Locate every malaria parasite and every leukocyte.
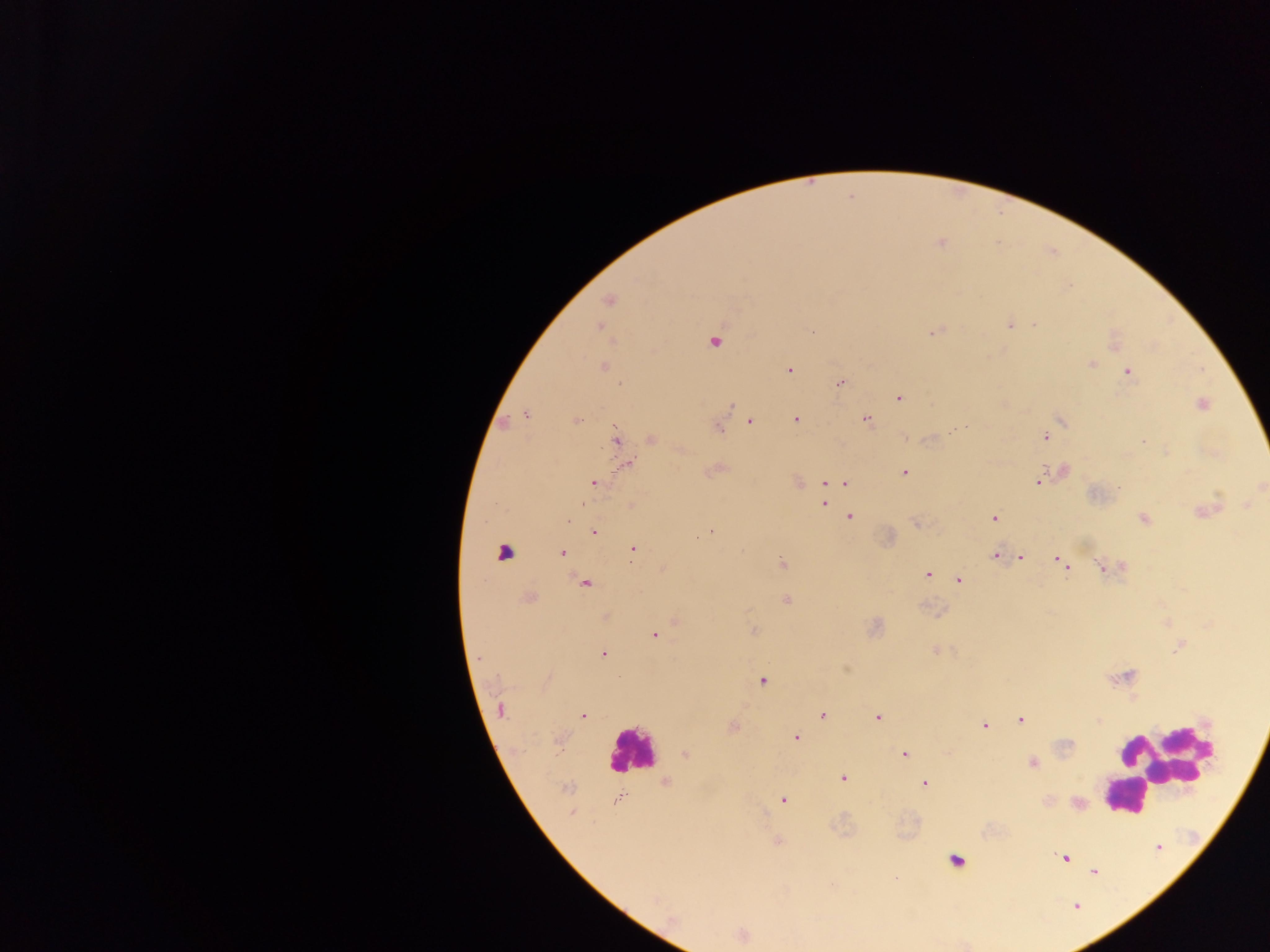
Approximate centers as x y in pixels.
Malaria parasites: 940 243; 609 301; 1009 325; 1035 325; 599 327; 932 332; 713 341; 1090 365; 604 367; 790 370; 1128 372; 841 383; 899 397; 1202 404; 731 405; 525 414; 796 419; 577 420; 866 420; 749 421; 1060 421; 717 428; 1046 437; 615 438; 652 439; 1143 442; 627 464; 903 473; 1038 481; 593 483; 798 483; 841 483; 827 484; 1261 486; 824 504; 1210 509; 850 516; 994 517; 1144 519; 710 531; 594 532; 699 537; 632 548; 562 552; 995 555; 1021 558; 782 563; 1063 563; 1102 567; 927 575; 959 580; 585 584; 528 598; 787 601; 754 630; 653 635; 1178 648; 604 653; 479 658; 762 681; 500 709; 823 714; 583 715; 877 718; 1020 720; 1099 721; 984 726; 795 737; 685 754; 904 754; 1032 763; 842 778; 665 783; 924 783; 567 788; 616 800; 783 800; 572 813; 1064 858; 1093 871.
Leukocytes: 505 550; 631 751; 1163 762; 1122 796; 955 861.

One field of view. Image is 1270×952 pixels. Photographed through a microscope with a mobile-phone camera. Thick blood film. Collected in Ghana.